Comment on the morphology of the red blood cells.
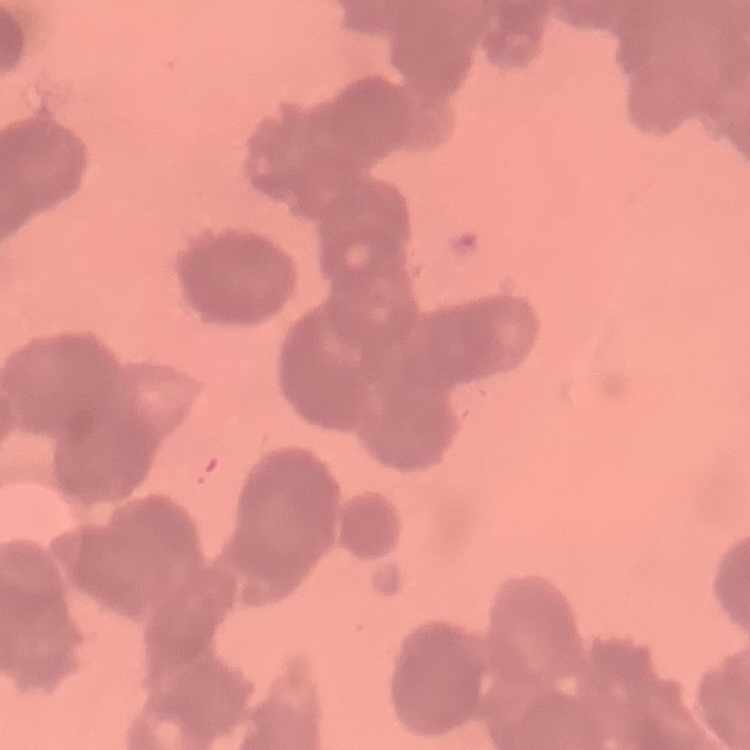

They show rouleaux formation.

Summary:
  - Preparation: thin blood film
  - Image type: one tile cut from a larger photomicrograph
  - Stain: Field's or Giemsa